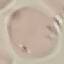

Result: negative for malaria parasites. Thin blood smear. Acquired by smartphone through the microscope eyepiece. Automatically extracted cell patch, resized to 64 × 64 pixels. Giemsa-stained preparation.